Assess this cell for malaria.
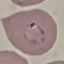

Parasitized.

Cell patch, automatically extracted from a larger field of view and resized to 64 × 64 pixels. Giemsa-stained preparation. Acquired by smartphone through the microscope eyepiece. Thin blood smear.